Classify this cell by malaria status.
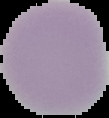
Uninfected.

From a thin blood film. The area outside the segmented cell region is set to black. Image is 109×118 pixels.